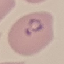
result = malaria parasites identified
capture = smartphone through the microscope eyepiece
preparation = thin blood smear
image type = cell patch, automatically extracted from a larger field of view and resized to 64 × 64 pixels
stain = Giemsa